State which parasite is depicted.
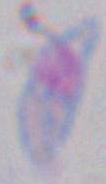
Toxoplasma gondii.

1000x magnification. Photomicrograph.